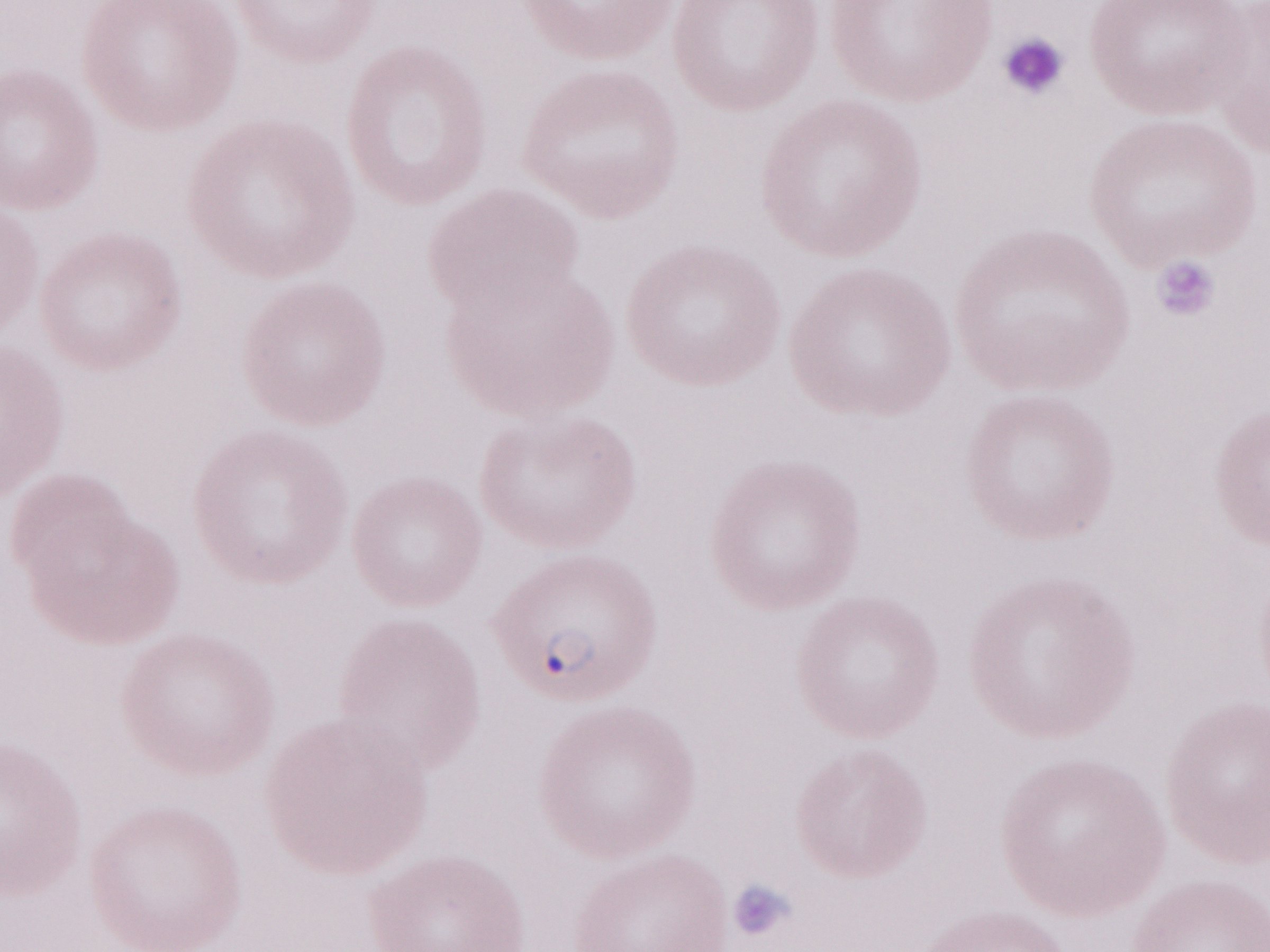 Olympus BX43 microscope, Olympus DP73 camera. Patient-level malaria diagnosis: positive. May-Grünwald-Giemsa stain. One field of this slide. Thin blood smear. Magnification: 1,000x. Image is 1270×952 pixels.